Point out each Plasmodium parasite.
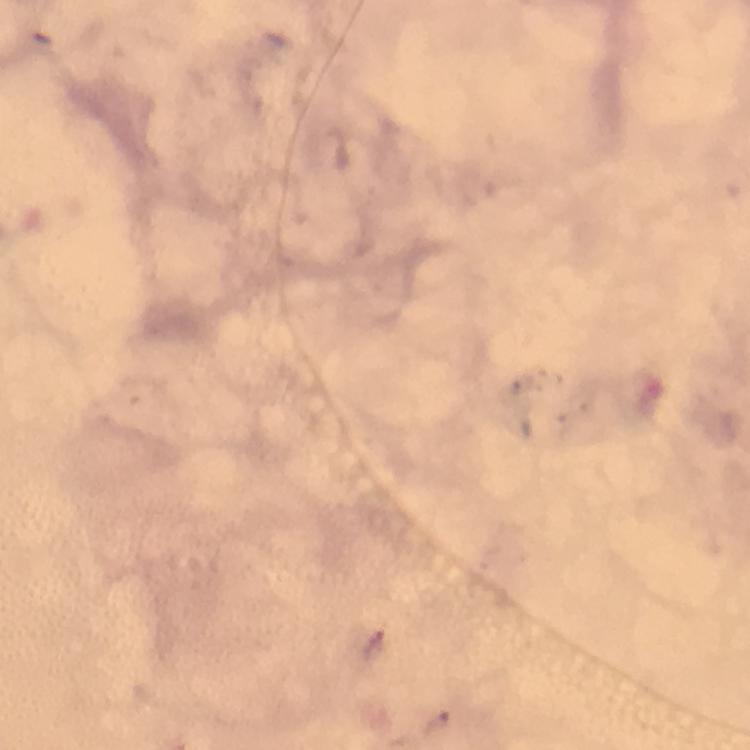
Approximate centers as [x, y] in pixels.
Plasmodium parasites: [438, 723].

Summary:
  - Image size: 750×750 pixels
  - Context: from a diagnostic examination for malaria
  - Magnification: 100x
  - Stain: Giemsa
  - Cropped from: one field of view
  - Preparation: thick blood film
  - Capture: smartphone mounted on the microscope
  - Immersion oil: applied